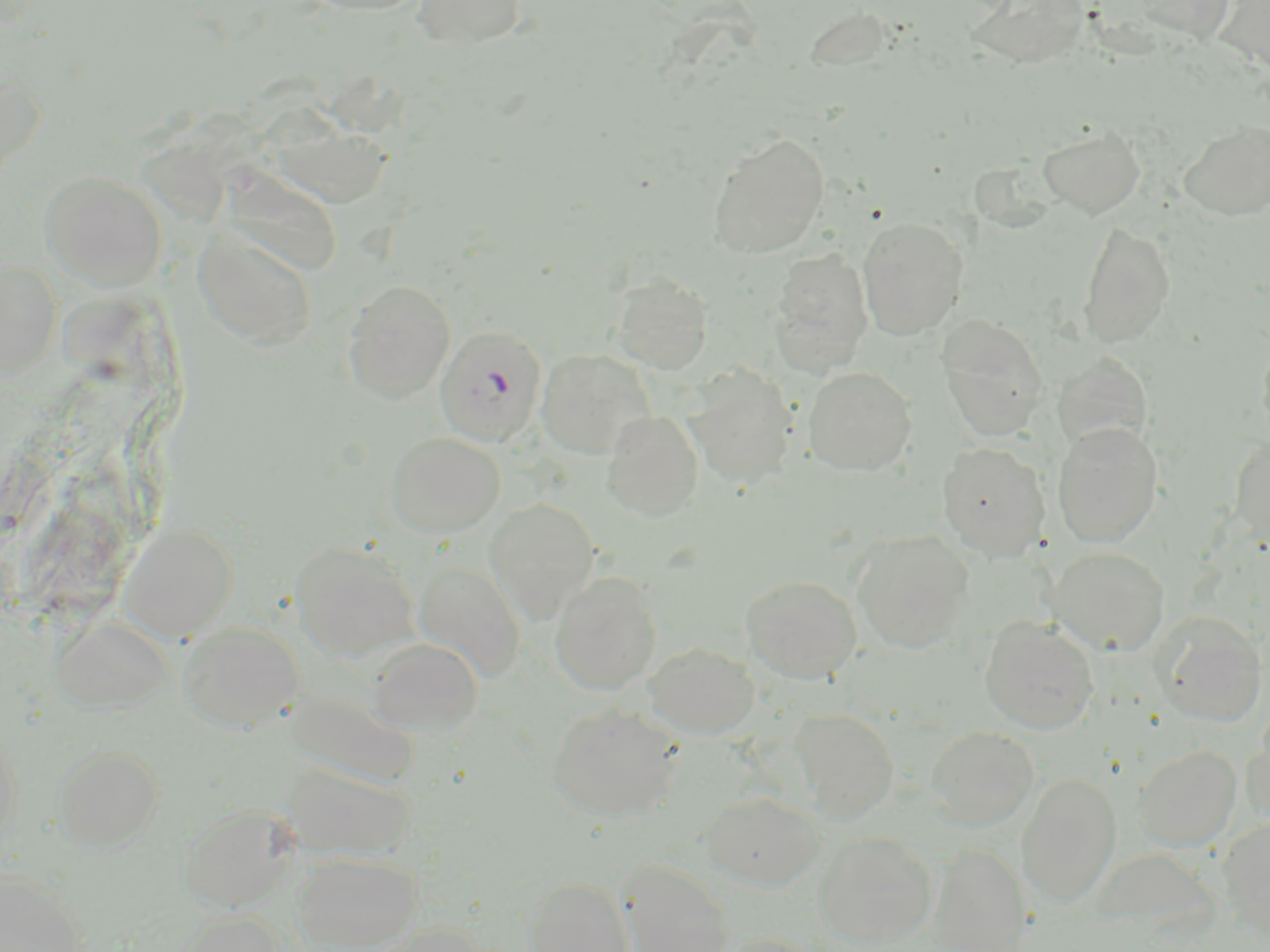

slide-level diagnosis = Plasmodium falciparum
image size = 1270×952 pixels
magnification = 1000x
stain = May-Grünwald-Giemsa
preparation = thin blood film
Plasmodium falciparum-infected red blood cell locations = approximate bounding boxes as named x1/y1/x2/y2 corners in pixels: (x1=436, y1=326, x2=547, y2=447)
field of view = single
modality = optical microscopy
uninfected red blood cell locations = approximate bounding boxes as named x1/y1/x2/y2 corners in pixels: (x1=297, y1=0, x2=432, y2=16), (x1=412, y1=0, x2=527, y2=49), (x1=967, y1=0, x2=1091, y2=69), (x1=0, y1=58, x2=46, y2=184), (x1=261, y1=116, x2=393, y2=208), (x1=1179, y1=121, x2=1270, y2=219), (x1=1038, y1=126, x2=1145, y2=218), (x1=708, y1=132, x2=829, y2=258), (x1=221, y1=169, x2=346, y2=277), (x1=41, y1=171, x2=167, y2=290), (x1=857, y1=216, x2=968, y2=339), (x1=1078, y1=221, x2=1175, y2=348), (x1=192, y1=225, x2=319, y2=351), (x1=768, y1=249, x2=874, y2=376), (x1=0, y1=260, x2=60, y2=377), (x1=611, y1=273, x2=713, y2=374), (x1=343, y1=279, x2=456, y2=403), (x1=937, y1=316, x2=1049, y2=441), (x1=1257, y1=329, x2=1270, y2=448), (x1=537, y1=349, x2=655, y2=459), (x1=1052, y1=353, x2=1153, y2=455), (x1=684, y1=366, x2=797, y2=489), (x1=803, y1=366, x2=916, y2=476), (x1=601, y1=410, x2=704, y2=520), (x1=1052, y1=423, x2=1162, y2=547), (x1=385, y1=432, x2=505, y2=538), (x1=1229, y1=435, x2=1270, y2=550), (x1=937, y1=442, x2=1050, y2=561), (x1=484, y1=498, x2=600, y2=620), (x1=118, y1=523, x2=238, y2=642), (x1=852, y1=530, x2=974, y2=653), (x1=290, y1=540, x2=421, y2=661), (x1=1047, y1=547, x2=1169, y2=655), (x1=413, y1=562, x2=525, y2=682), (x1=550, y1=571, x2=662, y2=694), (x1=741, y1=575, x2=862, y2=682), (x1=1154, y1=611, x2=1267, y2=726), (x1=49, y1=613, x2=173, y2=713), (x1=979, y1=617, x2=1099, y2=734), (x1=178, y1=622, x2=305, y2=732), (x1=368, y1=637, x2=483, y2=734), (x1=645, y1=642, x2=760, y2=738), (x1=285, y1=688, x2=419, y2=789), (x1=547, y1=703, x2=683, y2=821), (x1=790, y1=707, x2=898, y2=822), (x1=1240, y1=716, x2=1270, y2=829), (x1=0, y1=719, x2=23, y2=857), (x1=927, y1=726, x2=1039, y2=830), (x1=53, y1=745, x2=165, y2=850), (x1=1133, y1=745, x2=1241, y2=851), (x1=281, y1=763, x2=415, y2=861), (x1=1017, y1=772, x2=1121, y2=908), (x1=701, y1=793, x2=822, y2=890), (x1=177, y1=803, x2=301, y2=911), (x1=1218, y1=819, x2=1270, y2=938), (x1=813, y1=831, x2=938, y2=948), (x1=928, y1=843, x2=1029, y2=951), (x1=292, y1=851, x2=422, y2=951), (x1=618, y1=861, x2=735, y2=952), (x1=0, y1=871, x2=87, y2=952), (x1=524, y1=877, x2=635, y2=952), (x1=170, y1=909, x2=285, y2=952), (x1=358, y1=923, x2=493, y2=952), (x1=717, y1=933, x2=831, y2=952)